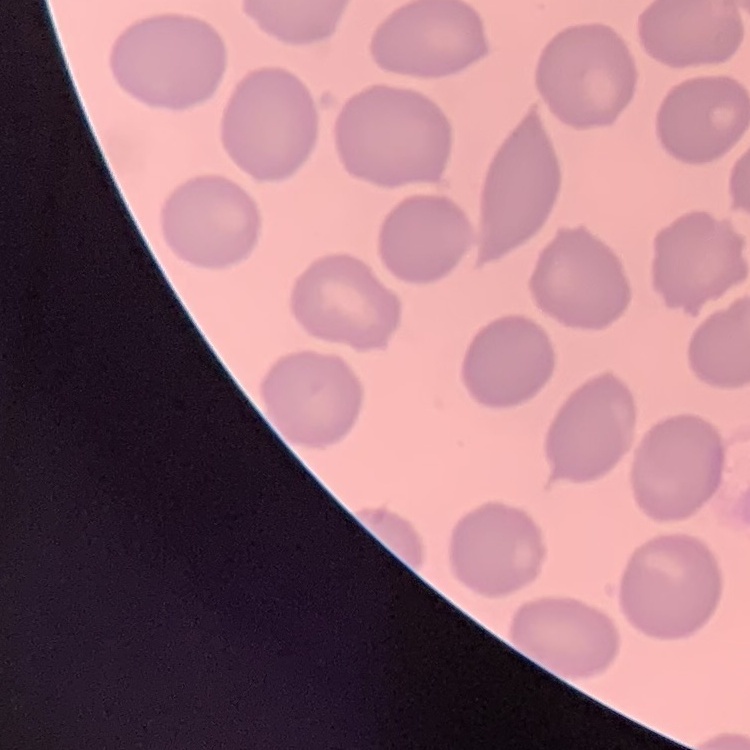

The erythrocytes show no rouleaux formation. Thin blood smear. Square crop of a larger photomicrograph. Stained with either Field's or Giemsa.